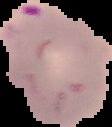
Summary:
  - Image type: cell region segmented out of the field of view; surrounding area masked to black
  - Image size: 112×127 pixels
  - Preparation: thin blood film
  - Result: Plasmodium parasites identified